Name the parasite shown.
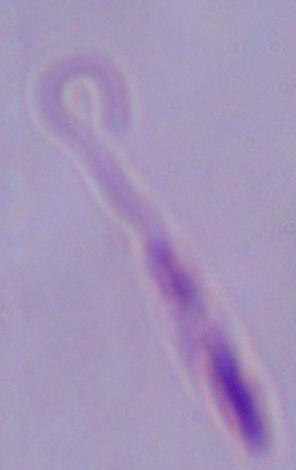
This is Leishmania.

Captured at 1000x magnification. Photomicrograph.